Outline each blood parasite and name the species.
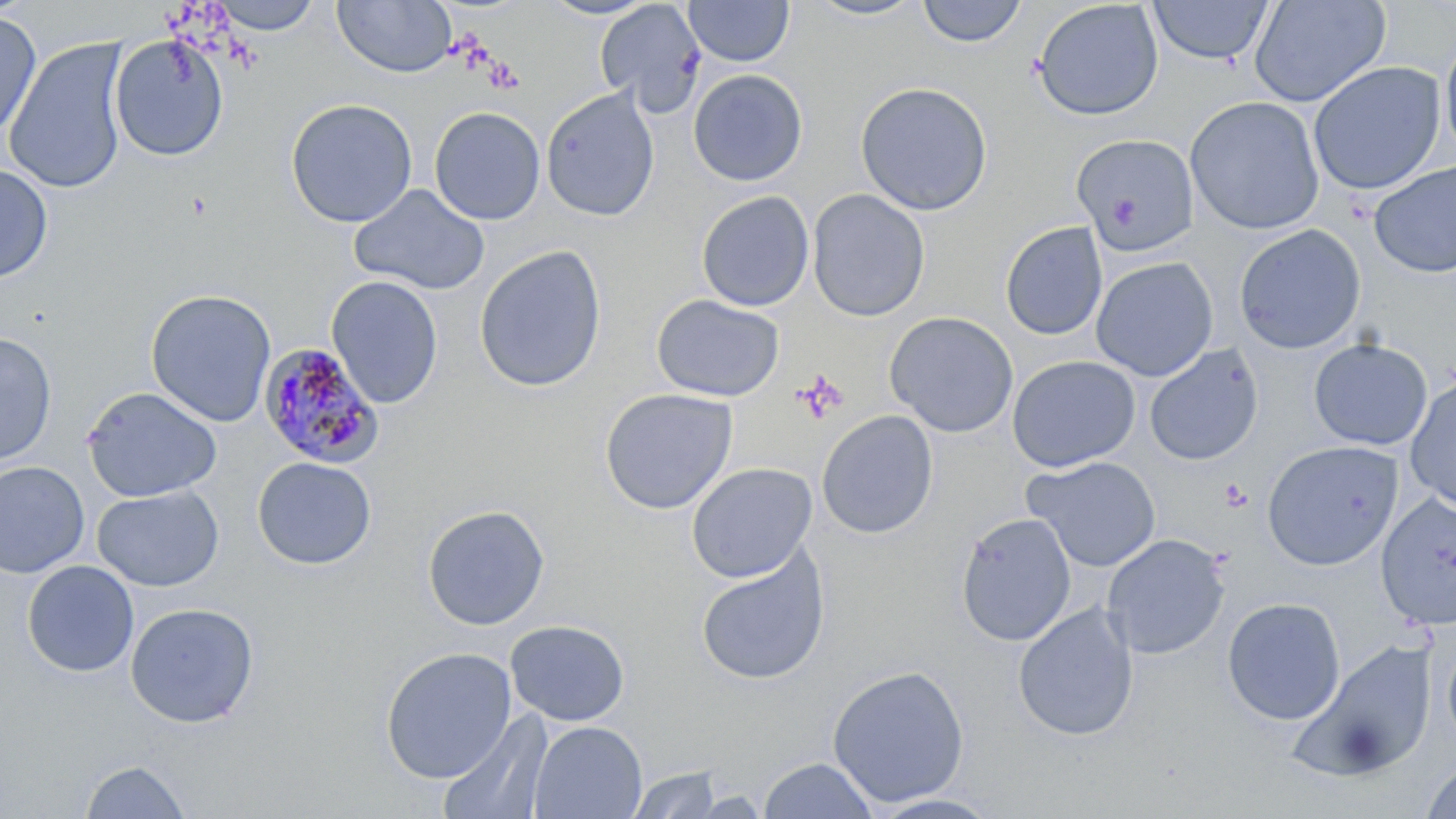

Approximate bounding boxes as [x1, y1, x2, y2] in pixels.
Plasmodium malariae-infected red blood cells: [258, 342, 386, 469].
No Plasmodium falciparum, Plasmodium ovale, Plasmodium vivax, Babesia divergens, or Trypanosoma brucei observed.

Summary:
  - Platelet locations: [1219, 478, 1252, 512]
  - Uninfected red blood cell locations: [209, 0, 325, 35], [332, 0, 457, 78], [536, 0, 660, 20], [804, 0, 925, 21], [594, 1, 707, 117], [683, 1, 795, 67], [916, 1, 1028, 48], [1147, 1, 1274, 66], [1249, 1, 1390, 107], [1032, 2, 1164, 121], [0, 11, 41, 142], [1439, 30, 1456, 169], [109, 34, 229, 161], [3, 37, 131, 194], [1308, 61, 1446, 195], [688, 69, 808, 187], [855, 81, 993, 216], [540, 86, 660, 222], [1185, 95, 1325, 235], [285, 97, 418, 228], [429, 106, 546, 225], [1071, 133, 1199, 256], [1369, 161, 1456, 279], [0, 163, 53, 283], [348, 183, 490, 296], [807, 188, 930, 322], [696, 190, 814, 311], [1000, 221, 1108, 341], [1233, 224, 1366, 354], [473, 244, 607, 393], [1090, 256, 1218, 381], [326, 276, 444, 409], [145, 288, 277, 428], [650, 294, 785, 402], [884, 311, 1019, 437], [0, 332, 58, 466], [1308, 338, 1433, 450], [1144, 344, 1264, 466], [1007, 355, 1141, 472], [1404, 378, 1456, 513], [82, 386, 222, 502], [599, 387, 739, 515], [816, 410, 939, 539], [1262, 440, 1403, 570], [252, 455, 376, 570], [1022, 455, 1162, 572], [0, 461, 90, 578], [686, 462, 818, 582], [91, 485, 224, 592], [1375, 492, 1456, 630], [422, 504, 550, 631], [954, 512, 1077, 646], [1101, 533, 1230, 660], [694, 548, 831, 686], [21, 560, 140, 678], [1222, 597, 1345, 725], [124, 602, 259, 728], [1012, 602, 1139, 741], [504, 619, 630, 726], [1442, 634, 1456, 750], [1290, 638, 1438, 782], [380, 646, 517, 784], [826, 665, 970, 807], [437, 712, 552, 819], [528, 720, 647, 819], [758, 756, 879, 818], [79, 759, 192, 818], [1421, 760, 1456, 819], [626, 765, 724, 818], [867, 793, 1003, 818]
  - Slide-level diagnosis: Plasmodium malariae
  - Magnification: 1000x
  - Preparation: thin blood film
  - Field of view: single
  - Image size: 1456×819 pixels
  - Stain: May-Grünwald-Giemsa
  - Modality: optical microscopy